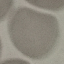
Summary:
  - Result: no malaria parasites seen
  - Image type: cell patch, automatically extracted from a larger field of view and resized to 64 × 64 pixels
  - Capture: smartphone through the microscope eyepiece
  - Preparation: thin blood film
  - Stain: Giemsa